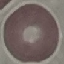
malaria_status: uninfected
image_type: cell patch, automatically extracted from a larger field of view and resized to 64 × 64 pixels
capture: smartphone camera at the microscope eyepiece
preparation: thin blood film
stain: Giemsa